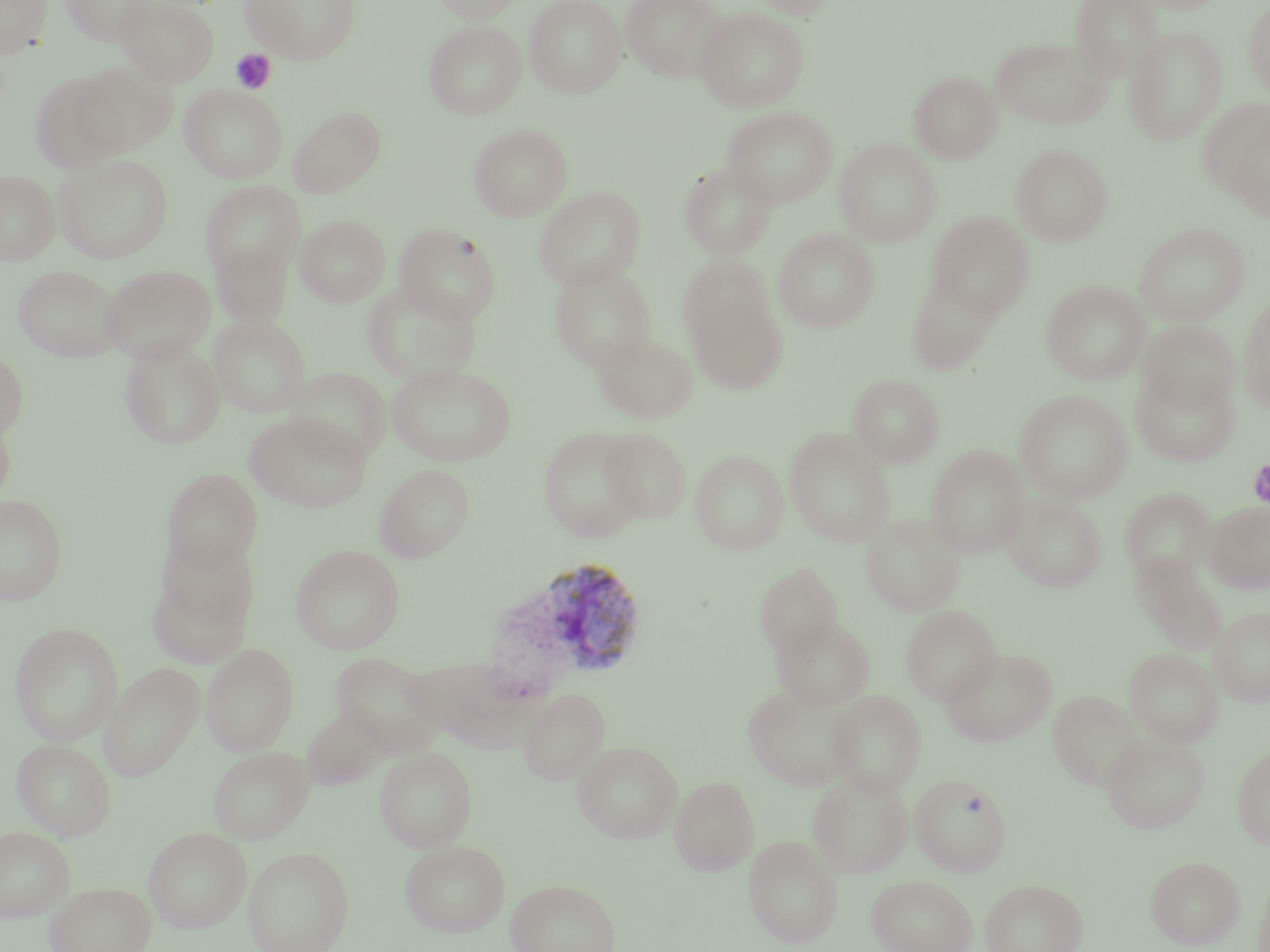

{
  "slide_level_diagnosis": "Plasmodium vivax",
  "preparation": "thin blood film",
  "magnification": "1000x",
  "platelet_locations": "approximate bounding boxes as [x1, y1, x2, y2] in pixels: [231, 49, 277, 94], [1247, 458, 1270, 510]",
  "plasmodium_vivax_infected_red_blood_cell_locations": "approximate bounding boxes as [x1, y1, x2, y2] in pixels: [514, 556, 650, 681]",
  "image_size": "1270×952 pixels",
  "modality": "light microscopy",
  "uninfected_red_blood_cell_locations": "approximate bounding boxes as [x1, y1, x2, y2] in pixels: [0, 0, 54, 60], [60, 0, 157, 45], [117, 0, 220, 87], [241, 0, 361, 64], [433, 0, 524, 23], [524, 0, 626, 98], [620, 0, 726, 82], [749, 0, 841, 18], [1070, 0, 1165, 80], [1131, 0, 1227, 14], [1243, 2, 1270, 99], [696, 7, 810, 112], [424, 20, 526, 119], [1124, 27, 1227, 146], [990, 36, 1112, 129], [70, 59, 178, 158], [29, 71, 126, 174], [909, 71, 1002, 163], [179, 84, 288, 183], [1199, 99, 1270, 210], [289, 106, 386, 197], [723, 107, 837, 207], [469, 123, 572, 221], [834, 138, 942, 247], [1011, 144, 1113, 246], [54, 154, 174, 263], [679, 162, 776, 258], [0, 170, 60, 264], [200, 180, 306, 282], [534, 187, 645, 290], [927, 212, 1035, 317], [296, 215, 391, 307], [1134, 222, 1250, 325], [394, 223, 501, 325], [774, 228, 879, 332], [211, 242, 292, 326], [679, 259, 784, 384], [14, 264, 123, 362], [101, 264, 216, 364], [550, 264, 656, 370], [907, 272, 1002, 375], [1041, 279, 1151, 385], [361, 281, 482, 386], [1238, 295, 1270, 414], [209, 315, 311, 418], [1138, 320, 1241, 415], [592, 332, 699, 423], [121, 342, 225, 449], [0, 347, 29, 442], [387, 363, 516, 466], [289, 367, 392, 465], [1131, 367, 1240, 467], [848, 373, 945, 467], [1014, 389, 1133, 503], [244, 411, 371, 512], [0, 412, 15, 512], [538, 427, 646, 542], [599, 427, 692, 523], [784, 429, 896, 547], [926, 445, 1030, 557], [691, 450, 788, 554], [375, 464, 474, 562], [163, 469, 262, 573], [1119, 488, 1216, 583], [1003, 493, 1108, 592], [0, 494, 68, 606], [1204, 501, 1270, 593], [860, 513, 965, 617], [151, 533, 261, 655], [290, 544, 406, 654], [1132, 557, 1225, 653], [754, 563, 844, 659], [901, 605, 1002, 705], [1210, 605, 1270, 707], [772, 616, 876, 711], [10, 622, 123, 746], [201, 643, 300, 756], [940, 647, 1057, 747], [1124, 648, 1223, 747], [331, 652, 445, 755], [401, 657, 521, 744], [99, 662, 205, 781], [742, 682, 857, 790], [518, 689, 610, 785], [1048, 689, 1144, 788], [826, 690, 927, 797], [303, 708, 389, 789], [1101, 733, 1209, 833], [12, 738, 117, 840], [573, 741, 682, 843], [208, 745, 314, 844], [375, 746, 477, 852], [1232, 747, 1270, 849], [808, 772, 913, 878], [910, 773, 1012, 876], [670, 776, 759, 875], [0, 826, 76, 921], [144, 827, 252, 932], [743, 834, 843, 948], [399, 839, 511, 937], [243, 847, 354, 952], [1146, 855, 1245, 949], [1254, 868, 1270, 952], [866, 874, 978, 952], [507, 878, 620, 952], [980, 878, 1088, 952], [44, 881, 156, 952]",
  "stain": "May-Grünwald-Giemsa",
  "field_of_view": "single"
}